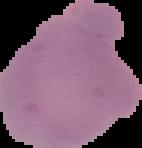

{
  "result": "Plasmodium parasites detected",
  "image_type": "segmented cell region on a black background",
  "image_size": "142×148 pixels",
  "preparation": "thin blood smear"
}